Evaluate for Plasmodium parasites.
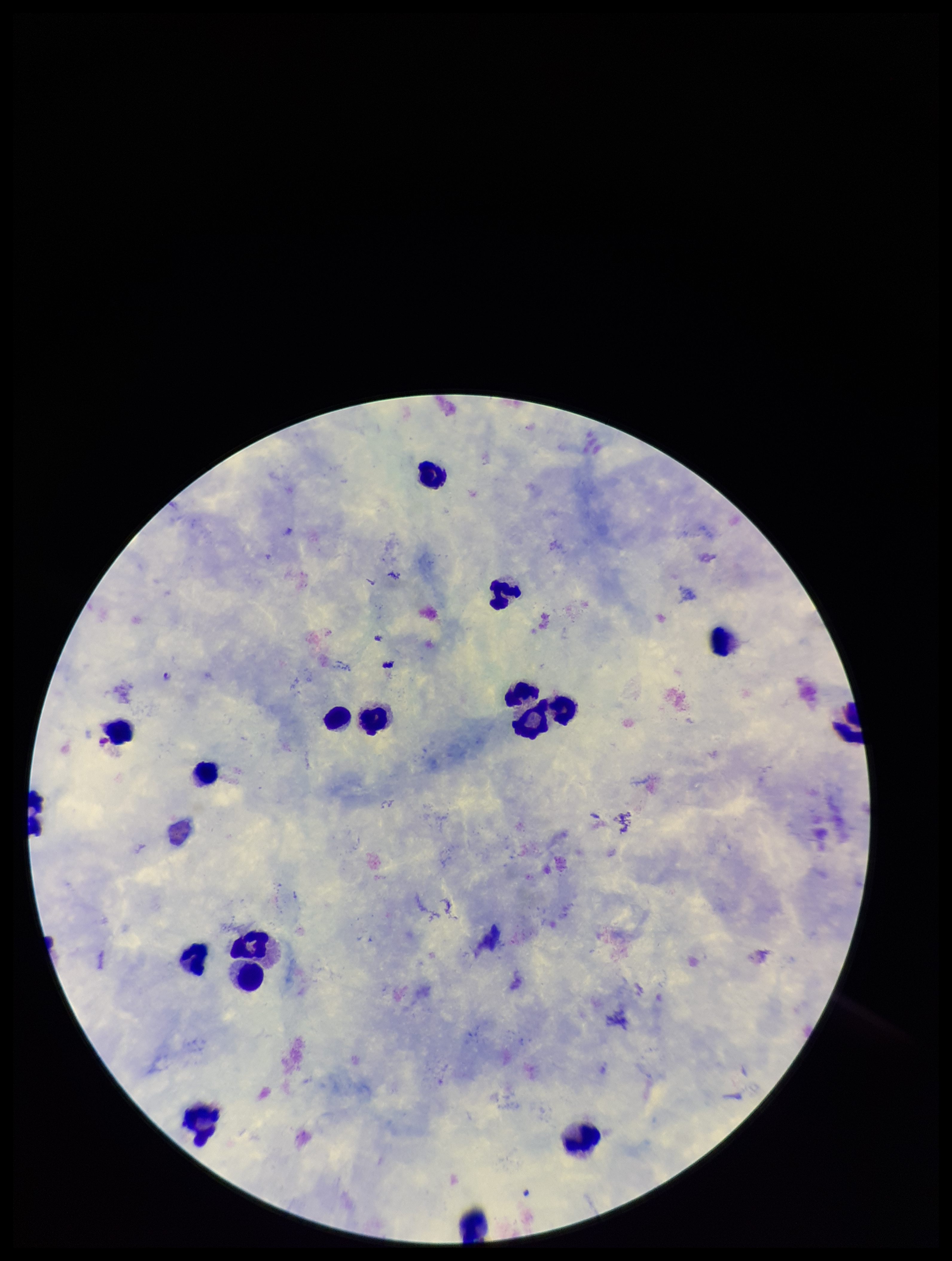

Detected.

Summary:
  - Preparation: thick
  - Leukocyte count: 18
  - Patient malaria status: positive
  - Species reported for this patient: Plasmodium falciparum
  - Field of view: one from this slide
  - Capture: smartphone photograph through the microscope eyepiece
  - Image size: 952×1261 pixels
  - Stain: Giemsa
  - Parasite count: 1